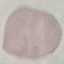
Result: no malaria parasites seen. Cell patch, automatically extracted from a larger field of view and resized to 64 × 64 pixels. Thin blood film. Photographed with a smartphone camera at the microscope eyepiece. Giemsa-stained preparation.